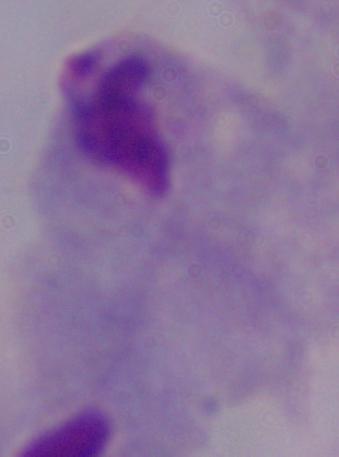

magnification = 1000x
identification = trichomonad
modality = micrograph